Locate the Plasmodium falciparum-infected red blood cells and any of indeterminate infection status.
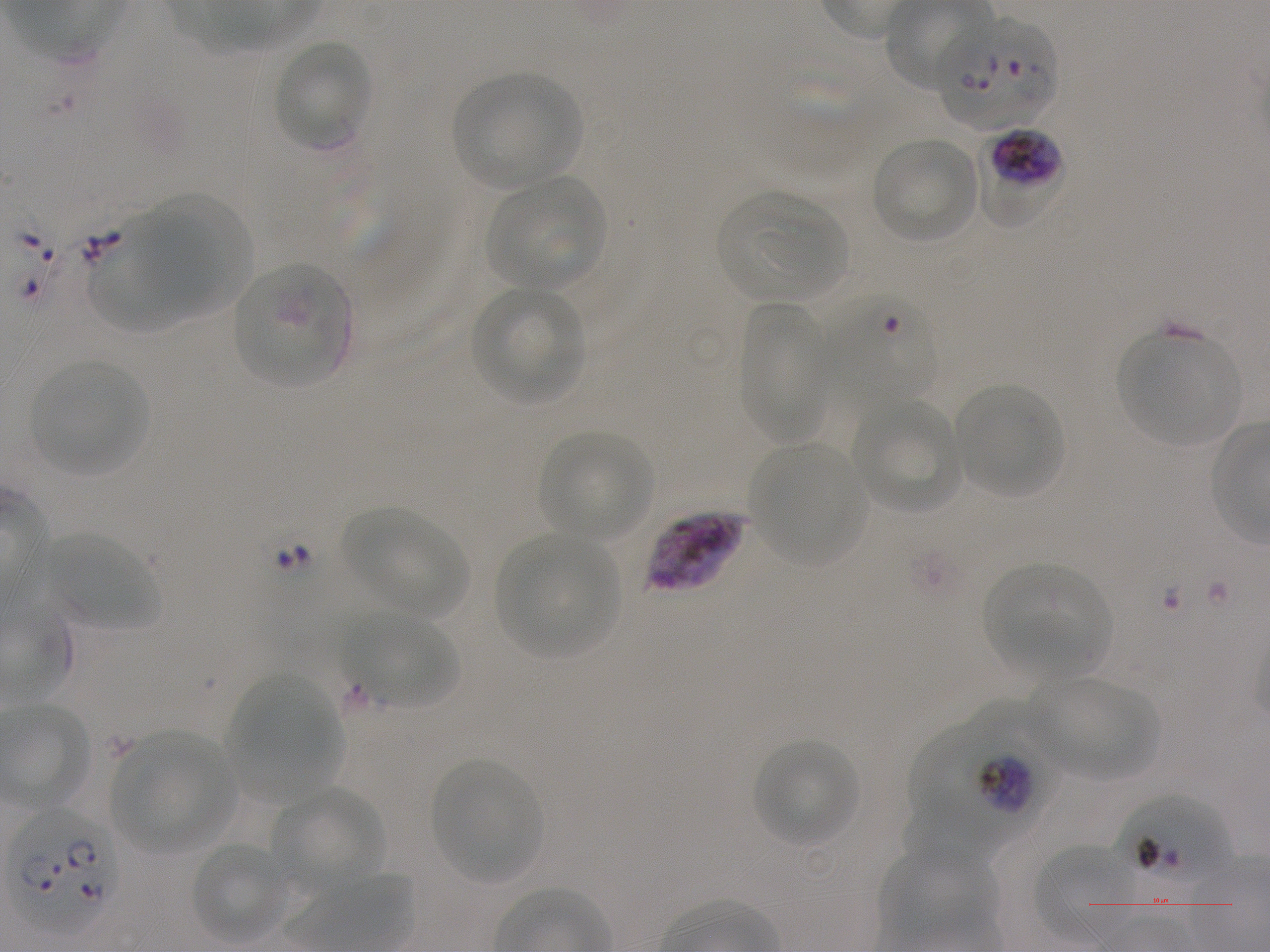
Approximate bounding boxes as (x1, y1, x2, y2) in pixels. Not every red blood cell is marked. A life-cycle stage — or a range of stages, where the recorded stages span more than one — follows each staged infected red blood cell.
Infected red blood cells: (939, 17, 1057, 130); (976, 129, 1066, 229) late trophozoite to late schizont; (915, 703, 1062, 837) trophozoite; (6, 808, 121, 935).
Red blood cells of indeterminate infection status: (815, 292, 938, 403), (646, 510, 746, 593), (1110, 793, 1232, 896).

Locations of uninfected red blood cells: (274, 40, 372, 148), (453, 72, 581, 188), (871, 137, 979, 243), (487, 177, 608, 290), (718, 192, 846, 300), (151, 196, 254, 317), (89, 222, 205, 332), (233, 262, 352, 389), (470, 288, 585, 405), (739, 302, 829, 444), (1118, 333, 1242, 446), (30, 360, 150, 475), (955, 384, 1066, 499), (851, 397, 959, 511), (539, 430, 654, 541), (752, 446, 863, 564), (347, 508, 467, 617), (496, 534, 618, 658), (46, 535, 160, 630), (984, 563, 1111, 674), (353, 616, 461, 710), (231, 676, 342, 790), (1027, 676, 1158, 781), (112, 734, 232, 851), (753, 739, 859, 845), (431, 761, 542, 883), (271, 787, 385, 894), (903, 797, 1000, 867), (190, 841, 289, 943), (1036, 844, 1133, 942), (879, 848, 995, 942). Giemsa-stained preparation. Image is 1270×952 pixels. Plasmodium falciparum strain NF54 in static in-vitro culture. Thin blood film. 100x oil-immersion objective, numerical aperture 1.25. Single field of view. Blood group of the donor: A+.